Rate the background quality.
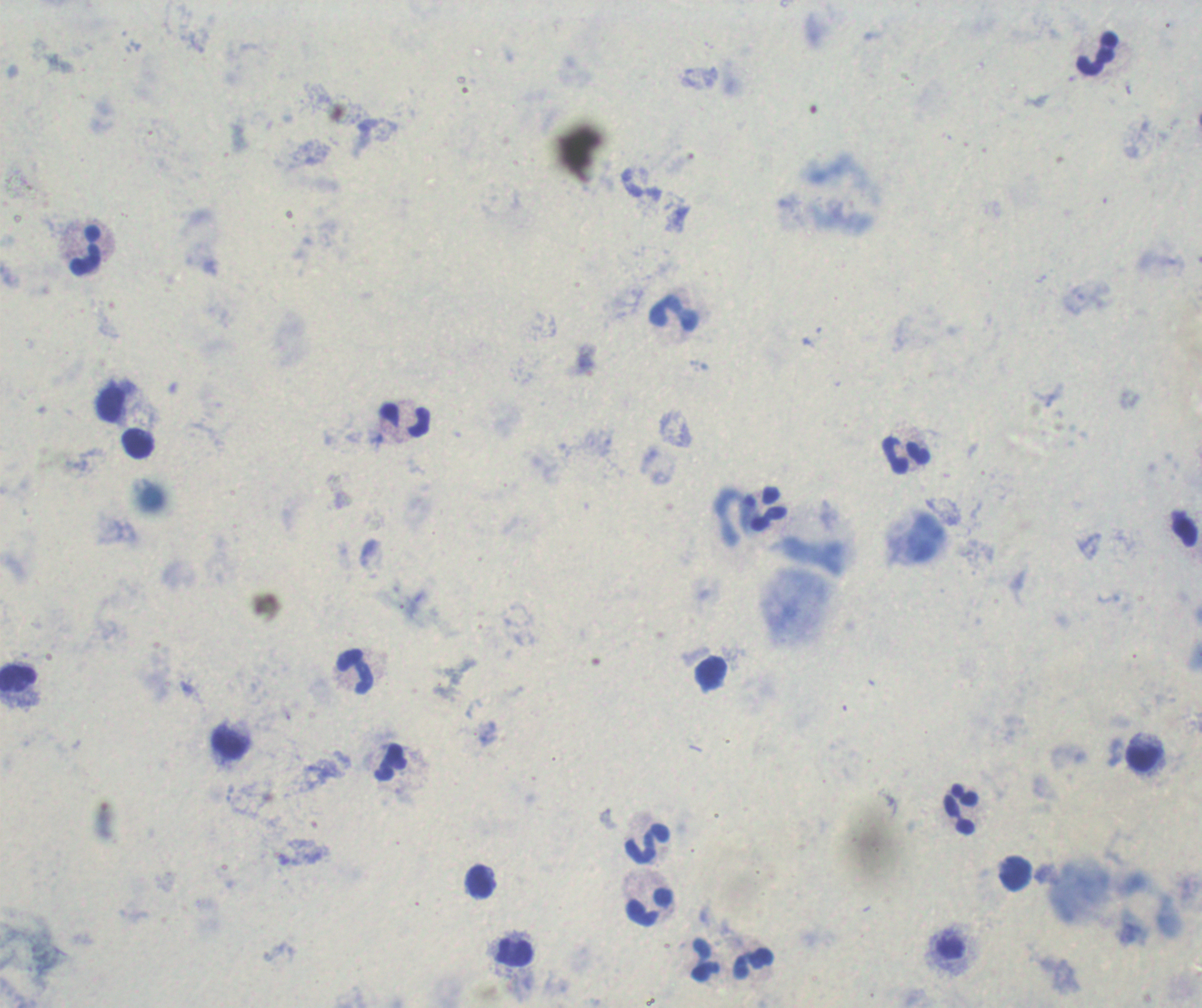
It is poor.

Approximate centers as [x, y] in pixels.
Summary:
  - Leukocyte locations: [1097, 55], [86, 250], [674, 314], [110, 403], [404, 419], [138, 443], [906, 454], [766, 509], [355, 672], [19, 680], [232, 743], [1142, 758], [392, 763], [961, 809], [648, 844], [1017, 874], [480, 880], [649, 908], [514, 951], [704, 960], [755, 963]
  - Preparation: thick blood smear
  - Field of view: single
  - Stain: Romanowsky
  - Magnification: 100x
  - Context: previously used in a real diagnosis
  - Result: no Plasmodium parasites detected
  - Image size: 1202×1008 pixels